Locate leukocytes (white blood cells).
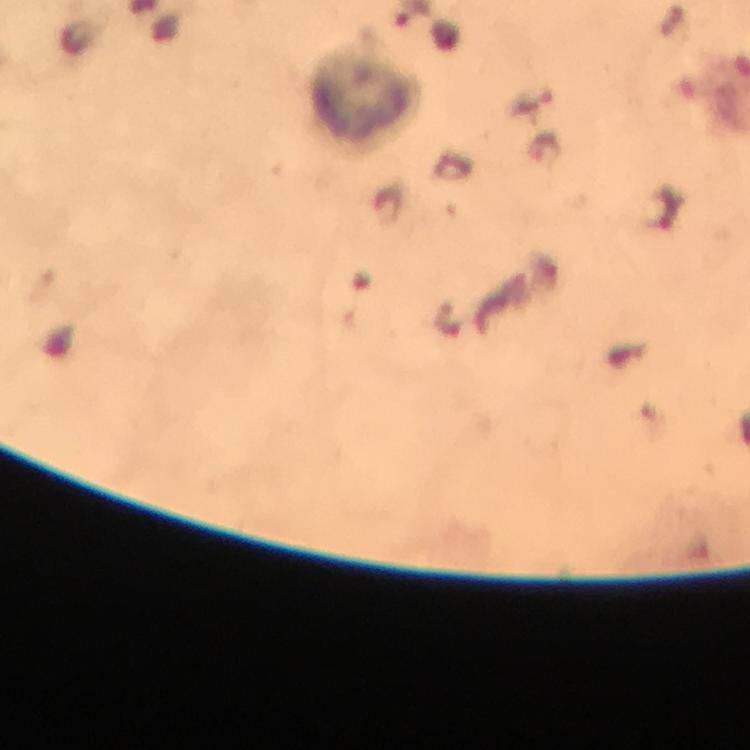

Approximate object centers, in pixels from the top-left corner.
Leukocytes: (x=363, y=99).

Cropped region of a single field of view. From a malaria diagnostic workup. Plasmodium parasites: none seen. Thick blood film. Image is 750×750 pixels. Giemsa-stained preparation. At 100x magnification. Photographed with a smartphone mounted on the microscope. Immersion oil applied.